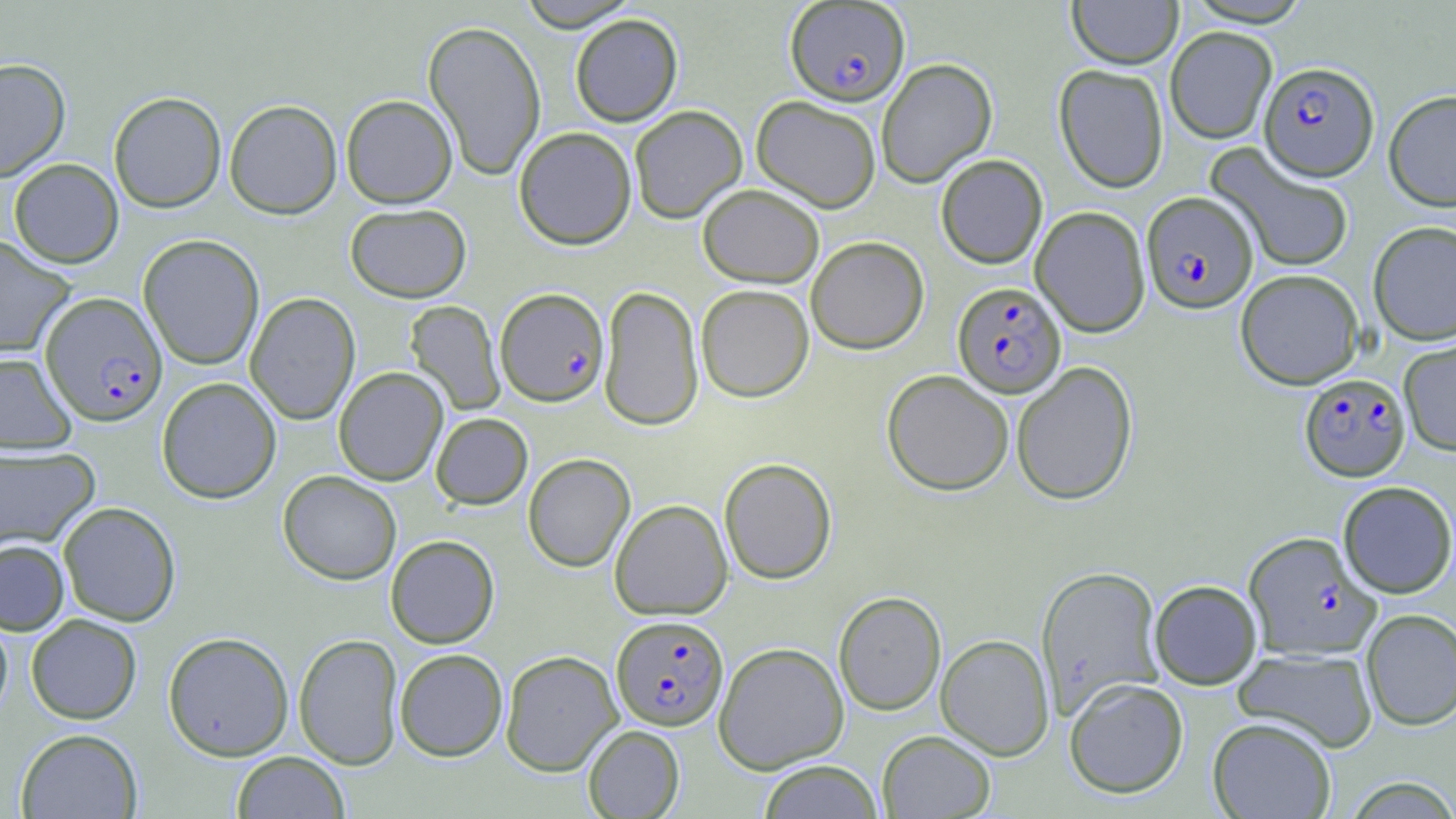
Approximate bounding boxes as (x1,y1)-(x2,y2) corner pairs in pixels. Plasmodium falciparum-infected red blood cell locations: (789,4)-(914,109), (1259,61)-(1379,181), (1141,191)-(1258,313), (953,281)-(1066,397), (495,287)-(609,406), (40,292)-(168,426), (1300,373)-(1411,482), (1242,531)-(1380,660), (611,615)-(728,730). Uninfected red blood cell locations: (516,0)-(641,31), (1183,0)-(1314,27), (1067,1)-(1182,69), (570,14)-(683,127), (423,19)-(546,180), (1165,26)-(1277,144), (0,58)-(70,181), (876,58)-(997,187), (1054,64)-(1169,193), (1384,89)-(1456,211), (108,91)-(226,213), (341,94)-(458,208), (751,95)-(881,213), (224,99)-(342,219), (629,105)-(747,223), (514,127)-(637,249), (1206,143)-(1356,274), (935,154)-(1047,269), (9,158)-(124,268), (697,183)-(824,287), (345,203)-(472,303), (1030,206)-(1150,337), (1367,220)-(1456,345), (138,234)-(265,370), (0,235)-(75,358), (806,236)-(929,354), (1235,268)-(1364,389), (696,284)-(813,402), (599,285)-(703,431), (245,292)-(361,425), (405,300)-(505,415), (1398,336)-(1456,456), (0,351)-(77,454), (1011,361)-(1138,505), (334,367)-(448,485), (882,369)-(1014,496), (156,377)-(281,504), (430,412)-(532,509), (0,446)-(99,552), (523,453)-(635,572), (718,457)-(837,584), (278,470)-(402,584), (1338,481)-(1456,598), (610,499)-(732,620), (58,501)-(181,626), (385,535)-(499,648), (0,539)-(69,635), (1036,565)-(1164,716), (1149,580)-(1262,689), (833,591)-(946,716), (0,608)-(14,723), (1361,609)-(1456,730), (26,614)-(142,724), (163,631)-(294,761), (294,633)-(403,770), (935,633)-(1055,760), (713,641)-(849,773), (394,648)-(508,761), (1233,648)-(1378,752), (500,650)-(622,776), (1064,677)-(1188,798), (1207,716)-(1336,819), (583,725)-(684,818), (15,728)-(143,818), (877,730)-(996,818), (231,751)-(349,818), (758,760)-(884,818), (1342,776)-(1456,818). Slide-level diagnosis: Plasmodium falciparum. Captured at 1000x magnification. Image is 1456×819 pixels. May-Grünwald-Giemsa stain. Light microscopy. One field of a larger specimen. Thin blood smear.